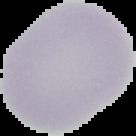 The area outside the segmented cell region is set to black. From a thin blood smear. Image is 136×136 pixels. Result: no Plasmodium parasites seen.